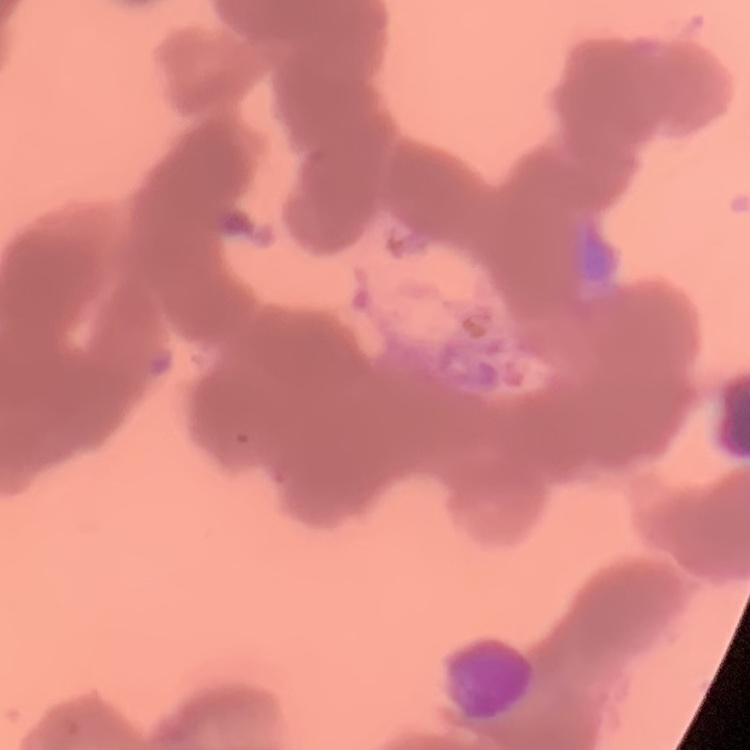

erythrocyte morphology = rouleaux formation
image type = one tile cut from a larger photomicrograph
preparation = thin blood smear
stain = Field's or Giemsa